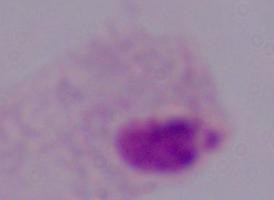
Summary:
  - Magnification: 1000x
  - Identification: trichomonad
  - Modality: micrograph